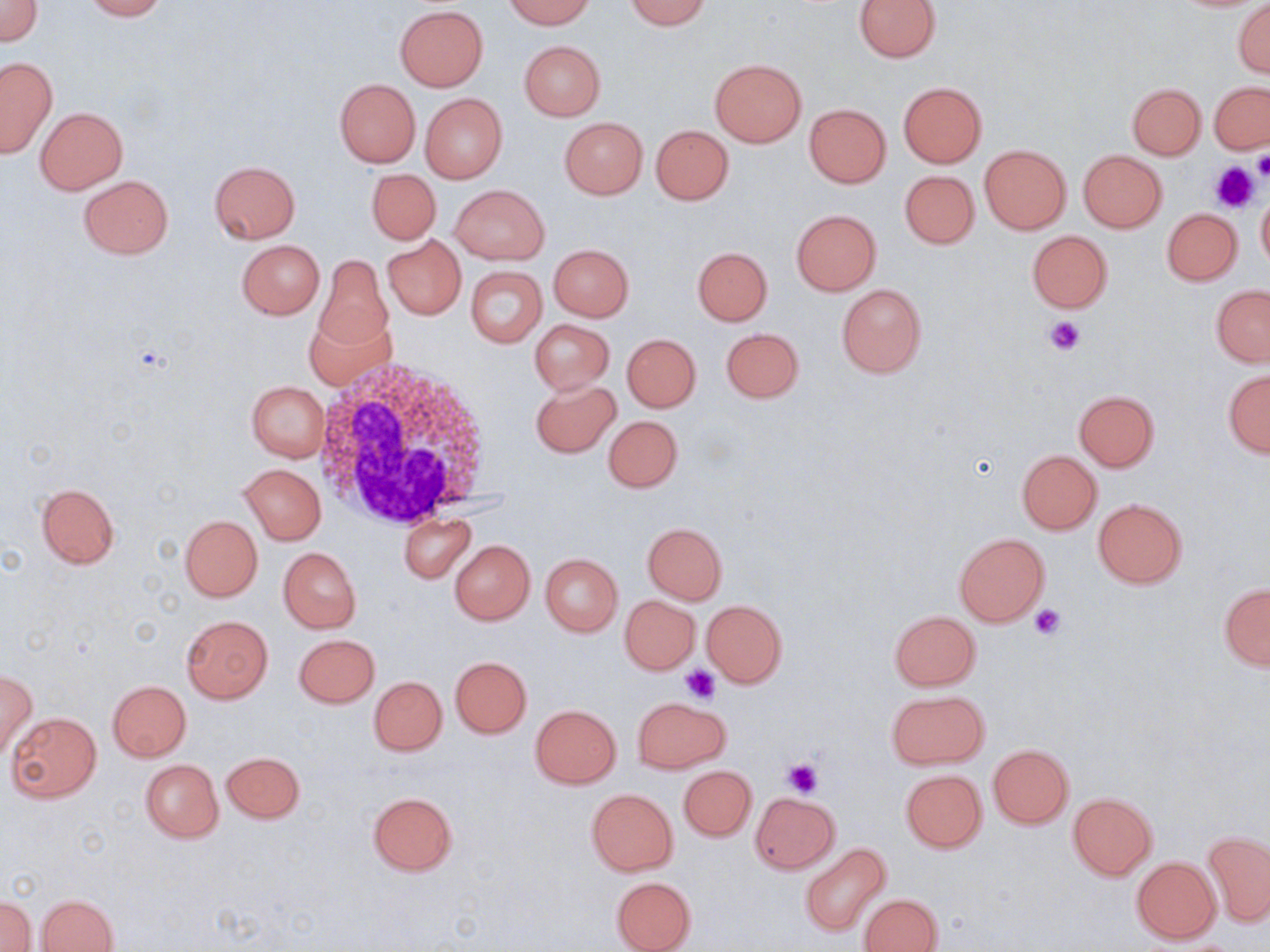

Approximate bounding boxes as (x1, y1, x2, y2) in pixels. Uninfected red blood cell locations: (81, 0, 166, 20), (504, 0, 594, 28), (625, 0, 712, 29), (854, 0, 941, 61), (1, 1, 43, 46), (1232, 1, 1270, 77), (395, 6, 488, 90), (518, 40, 604, 120), (0, 56, 57, 157), (709, 58, 807, 146), (334, 78, 421, 167), (1208, 81, 1270, 153), (898, 82, 987, 167), (1126, 83, 1206, 159), (421, 93, 507, 183), (804, 103, 891, 187), (35, 107, 128, 194), (559, 116, 647, 199), (651, 124, 734, 204), (980, 145, 1070, 233), (1078, 150, 1167, 231), (209, 160, 301, 245), (367, 169, 440, 245), (900, 170, 979, 249), (77, 175, 173, 259), (450, 184, 549, 263), (1257, 194, 1270, 272), (1161, 207, 1242, 285), (791, 210, 880, 295), (1027, 230, 1112, 312), (383, 236, 465, 318), (236, 239, 325, 319), (549, 244, 634, 320), (693, 247, 772, 325), (314, 255, 392, 352), (464, 266, 547, 348), (837, 284, 926, 377), (1211, 284, 1270, 366), (305, 313, 395, 390), (530, 319, 615, 395), (721, 327, 804, 404), (622, 333, 702, 412), (1223, 370, 1270, 457), (529, 378, 620, 457), (247, 380, 329, 461), (1074, 390, 1158, 471), (603, 415, 682, 493), (1017, 450, 1102, 534), (239, 463, 326, 545), (37, 482, 120, 567), (1092, 499, 1188, 588), (180, 515, 262, 601), (401, 515, 476, 583), (642, 521, 728, 605), (954, 532, 1050, 627), (449, 539, 535, 625), (278, 547, 360, 633), (541, 553, 622, 636), (1220, 583, 1270, 670), (620, 595, 699, 673), (701, 600, 787, 688), (889, 610, 981, 690), (181, 616, 273, 703), (293, 634, 379, 707), (450, 656, 532, 738), (0, 670, 38, 758), (370, 676, 446, 755), (107, 680, 190, 761), (886, 690, 989, 769), (634, 696, 726, 774), (530, 704, 621, 788), (7, 712, 101, 804), (986, 744, 1074, 829), (222, 752, 305, 823), (140, 759, 223, 842), (678, 765, 756, 841), (899, 769, 986, 853), (586, 788, 679, 875), (366, 791, 459, 878), (749, 792, 838, 873), (1068, 792, 1157, 879), (1204, 831, 1270, 927), (799, 842, 892, 937), (1132, 857, 1221, 944), (611, 876, 697, 952), (861, 893, 943, 952), (38, 895, 117, 951), (1, 896, 37, 952). Platelet locations: (1253, 151, 1270, 182), (1211, 161, 1261, 214), (1044, 315, 1084, 356), (1029, 603, 1067, 641), (679, 667, 720, 705), (784, 758, 822, 797). White blood cell locations: (315, 360, 499, 532). Slide-level diagnosis: negative for blood parasites. Image is 1270×952 pixels. Single field of view. Optical microscopy. May-Grünwald-Giemsa stain. Captured at 1000x magnification. Thin blood film.